Assess the morphology of the red blood cells.
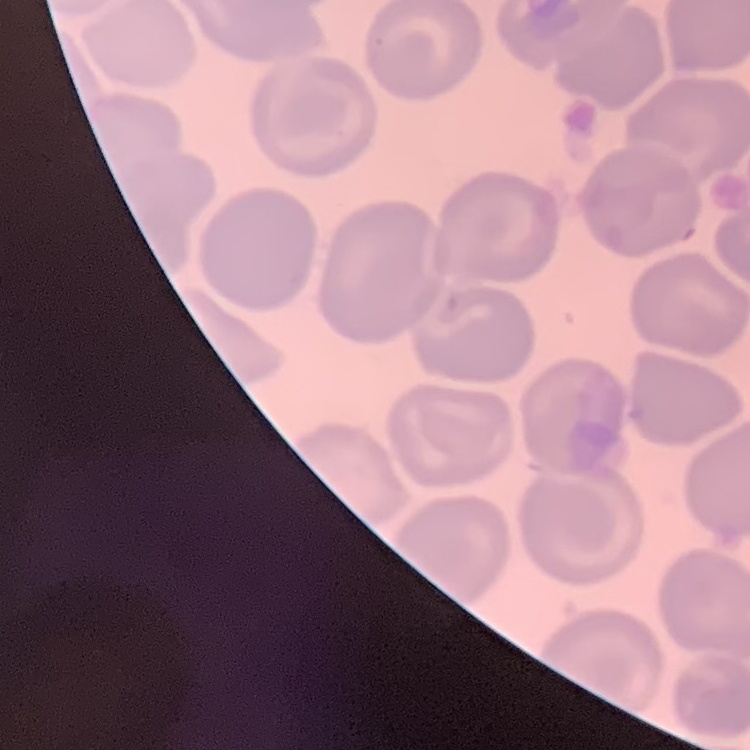

No rouleaux formation.

stain: Field's or Giemsa
image_type: one tile cut from a larger photomicrograph
preparation: thin blood film